Report the malaria status.
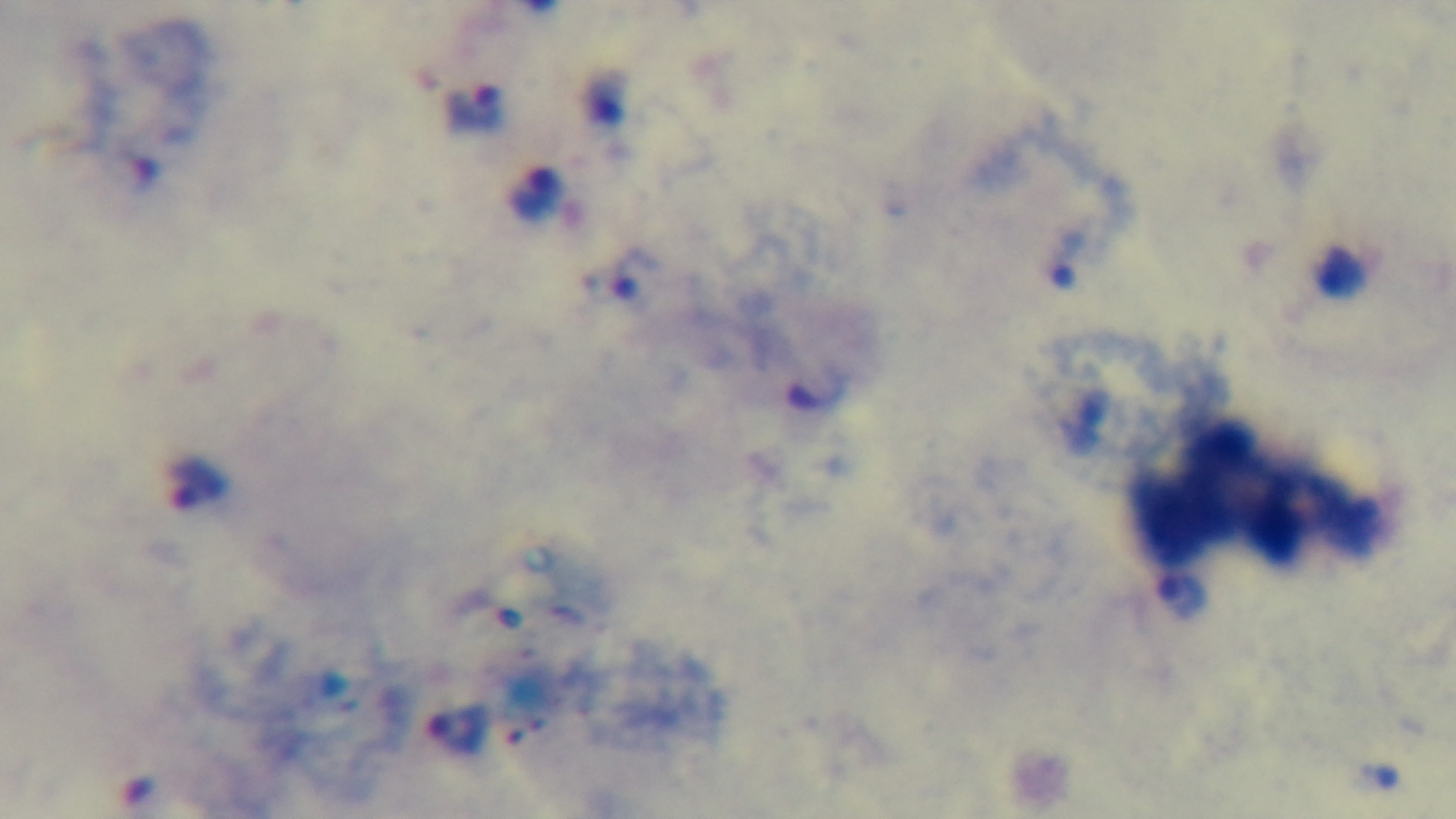
Positive.

100x oil-immersion objective. One field from the slide. Captured with a mounted 4K digital camera. Photomicrograph. Preparation: thick smear. Giemsa stain.